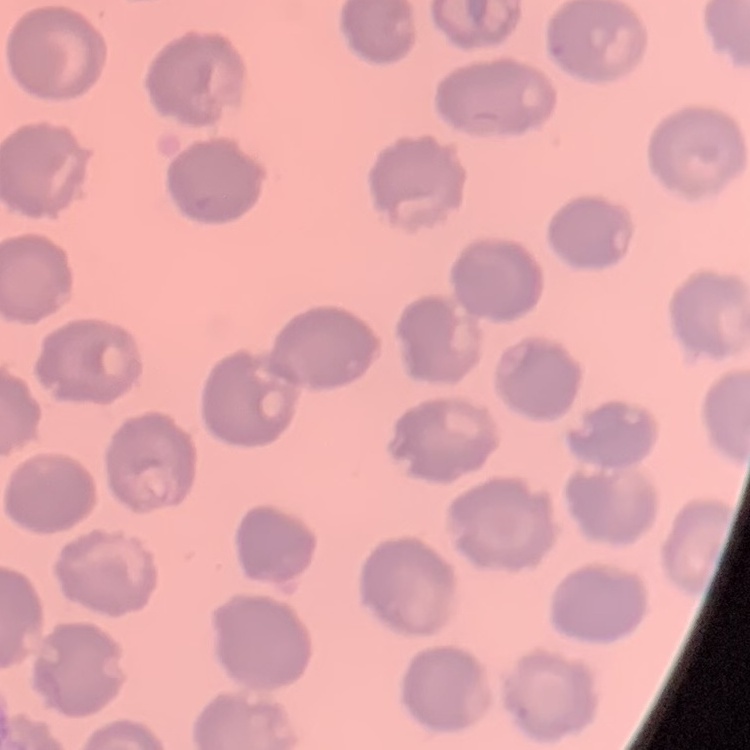
Summary:
  - Red blood cell morphology: no rouleaux formation
  - Image type: one tile cut from a larger photomicrograph
  - Stain: Field's or Giemsa
  - Preparation: thin peripheral smear